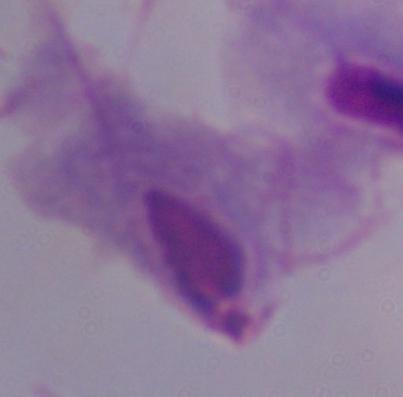

Summary:
  - Modality: micrograph
  - Identification: trichomonad
  - Magnification: 1000x